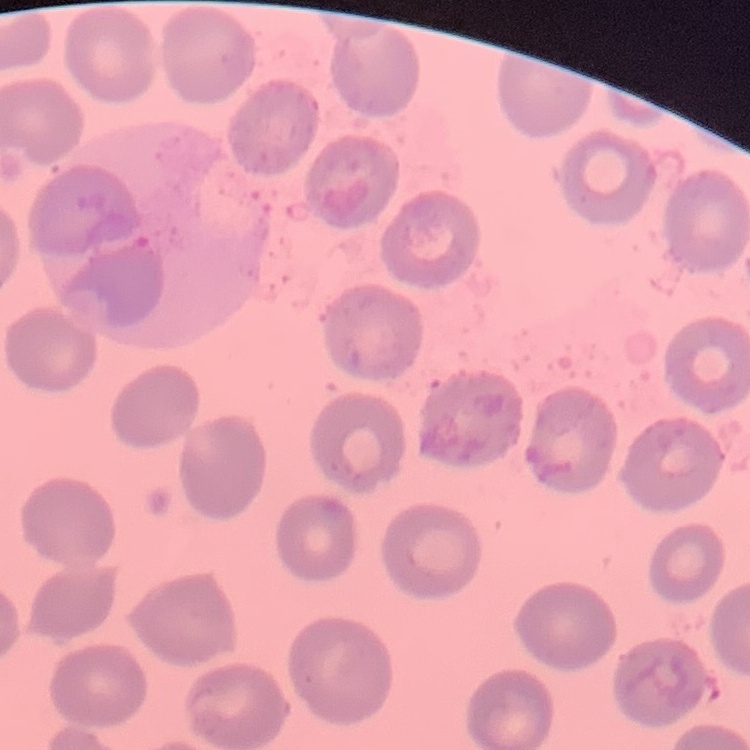

red blood cell morphology = no rouleaux formation
preparation = thin blood smear
stain = Field's or Giemsa
image type = one tile cut from a larger photomicrograph